Assess the morphology of the erythrocytes.
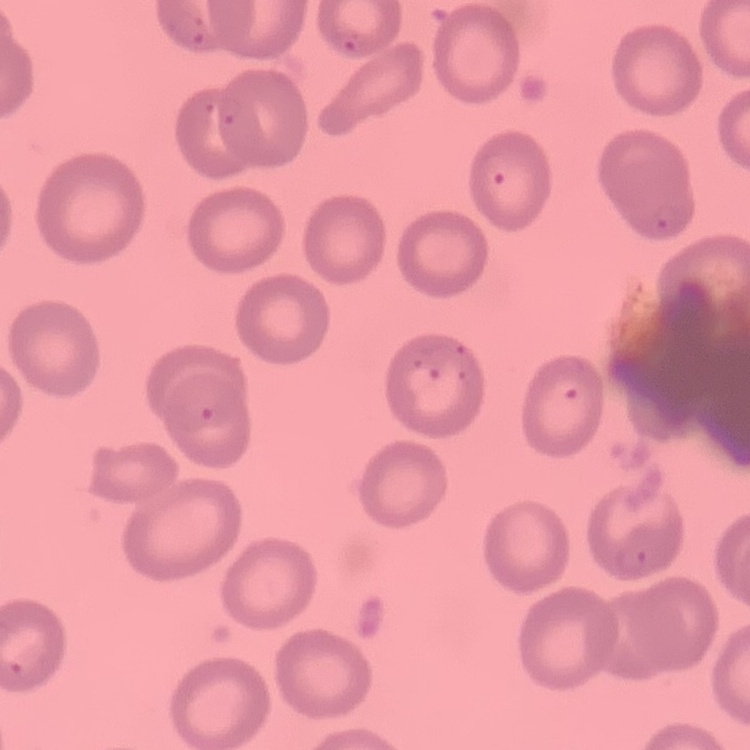

They show no rouleaux formation.

Summary:
  - Preparation: thin peripheral smear
  - Image type: square crop of a larger photomicrograph
  - Stain: Field's or Giemsa